Give a bounding box for every leukocyte visible.
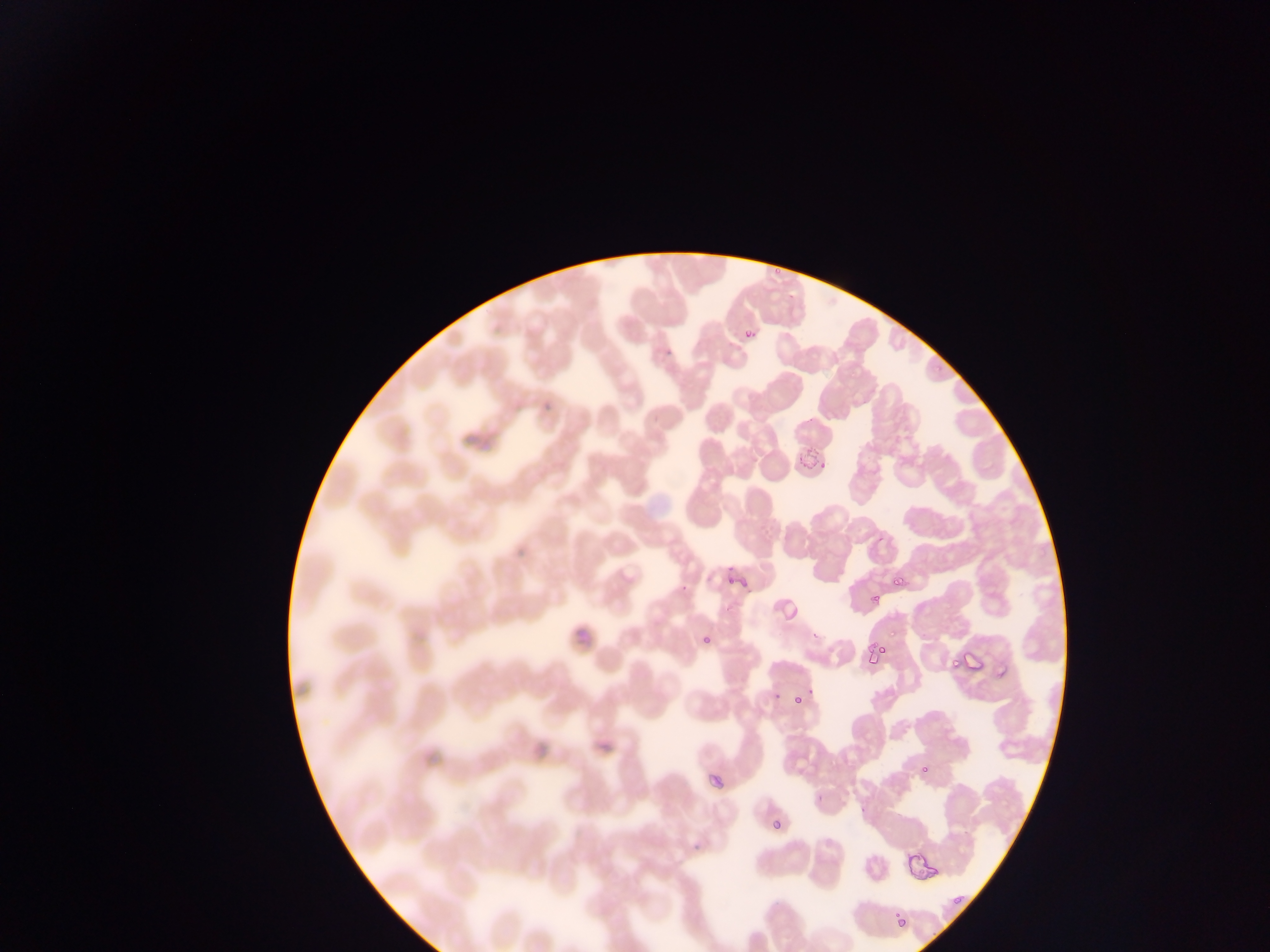

No leukocytes observed.

Approximate bounding boxes as left top right bottom in pixels. Malaria parasite locations: 769 264 788 276; 788 286 800 300; 738 325 758 350; 544 405 568 422; 791 435 834 476; 464 441 484 461; 513 519 524 567; 873 532 891 550; 720 550 751 593; 888 563 916 593; 672 577 689 592; 783 591 817 619; 862 591 885 609; 723 595 738 612; 571 604 595 647; 700 623 722 643; 860 630 897 687; 812 631 826 641; 962 648 982 671; 944 657 961 674; 770 689 780 703; 783 694 811 714; 532 738 554 761; 593 738 616 779; 908 757 937 790; 703 761 734 797; 815 785 830 810; 856 799 883 819; 767 816 786 856; 687 835 713 865; 903 843 938 883; 947 890 962 913; 892 904 918 932. Mobile-phone photograph taken through the microscope. Collected in Ghana. Image is 1270×952 pixels. Single field of view. Thin blood film.